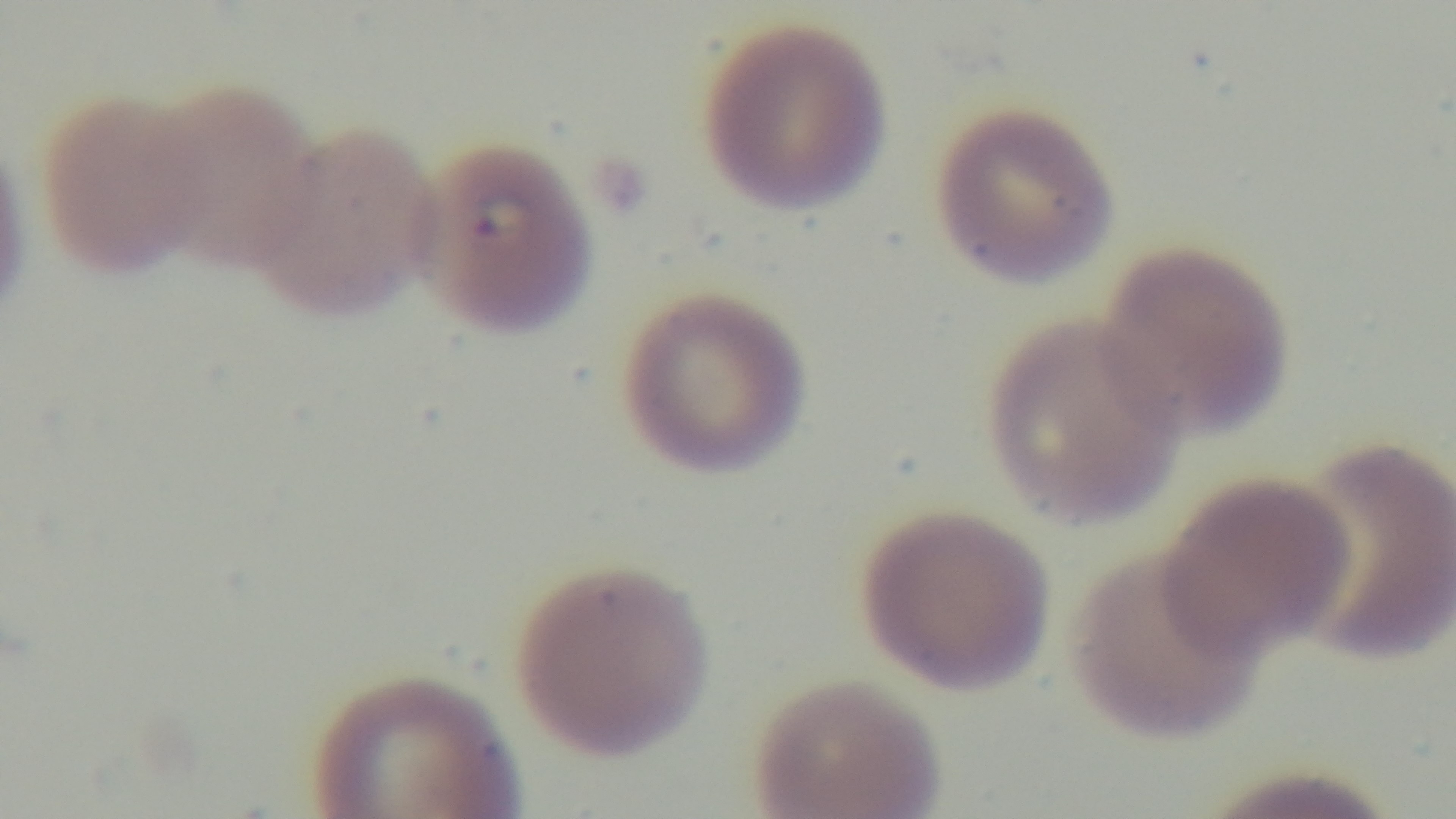
Single field of view. Malaria status: infected. Mounted 4K digital camera. Giemsa-stained. Photomicrograph. Oil-immersion objective, 100x. Preparation: thin smear.